Give the position of every leukocyte visible.
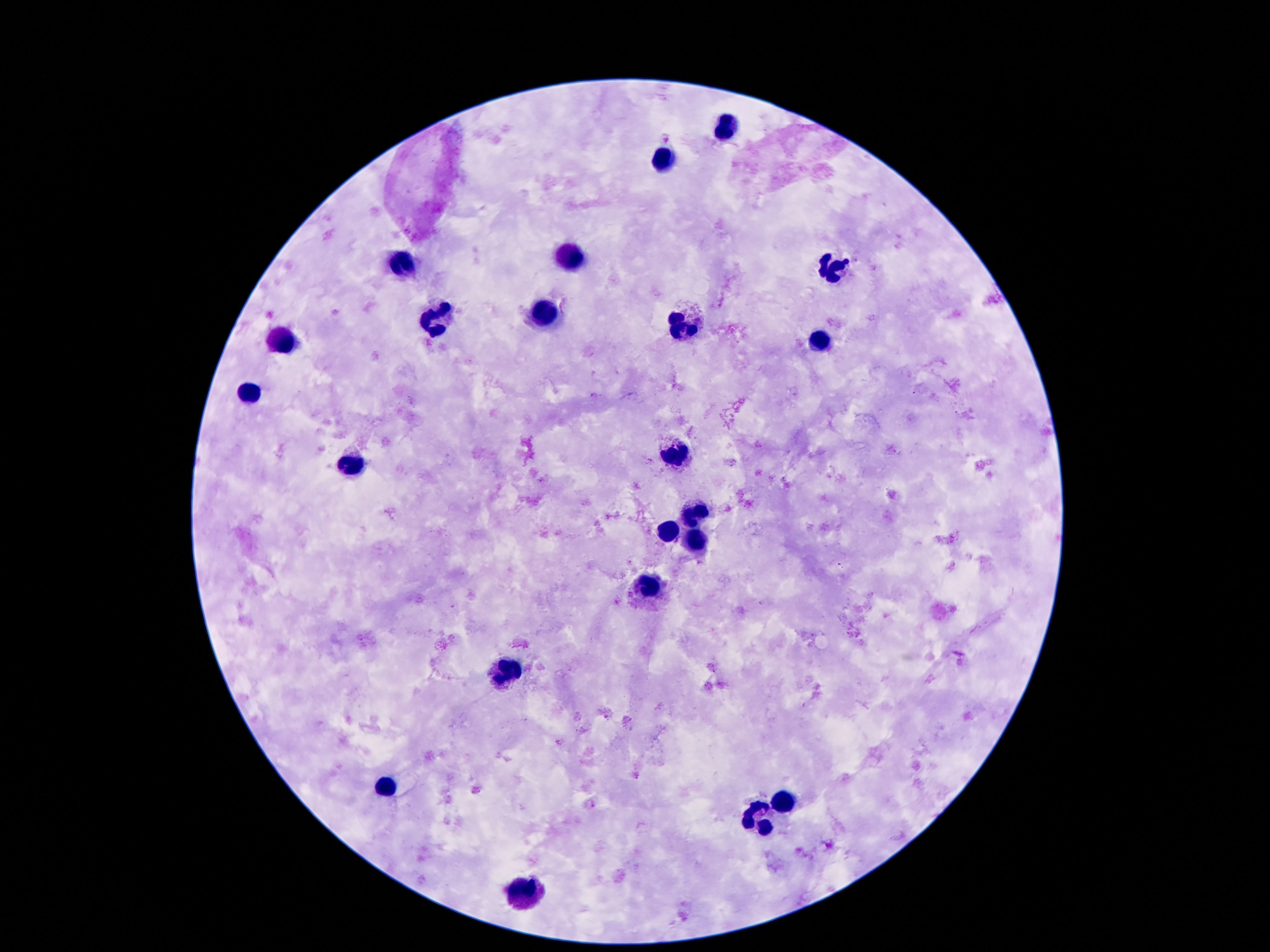

Approximate centers as [x, y] in pixels.
Leukocytes: [725, 127], [660, 160], [568, 256], [399, 260], [831, 268], [545, 313], [437, 320], [682, 325], [278, 342], [824, 344], [250, 393], [676, 453], [348, 466], [694, 516], [667, 533], [694, 536], [646, 583], [508, 670], [385, 790], [781, 804], [760, 819], [516, 893].

Summary:
  - Preparation: thick peripheral-blood smear
  - Field of view: single
  - Stain: Giemsa
  - Capture: smartphone camera through the microscope eyepiece
  - Patient malaria status: not infected
  - Magnification: 100x
  - Image size: 1270×952 pixels